Outline platelets.
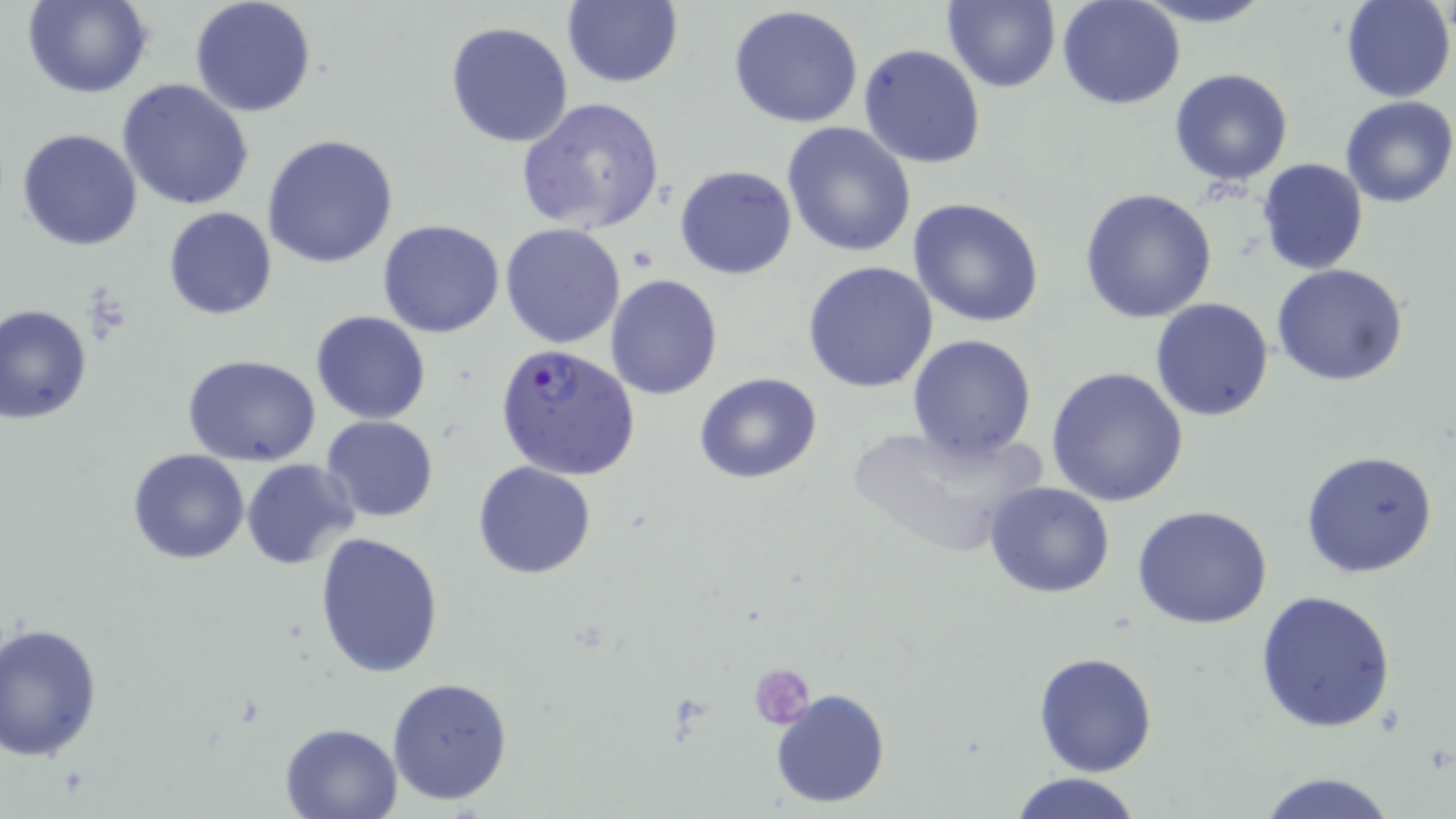
Approximate bounding boxes as (x1, y1, x2, y2) in pixels.
Platelets: (749, 662, 816, 729).

Plasmodium falciparum-infected red blood cell locations: (495, 343, 641, 479). Uninfected red blood cell locations: (24, 0, 152, 99), (188, 0, 317, 119), (561, 0, 683, 89), (940, 0, 1060, 92), (1056, 0, 1186, 111), (1128, 0, 1276, 28), (1340, 0, 1453, 103), (728, 6, 865, 128), (445, 21, 574, 149), (858, 43, 986, 168), (1169, 68, 1295, 186), (117, 79, 256, 212), (516, 96, 666, 235), (1339, 96, 1456, 207), (782, 122, 916, 257), (16, 127, 144, 250), (263, 133, 399, 268), (1258, 158, 1369, 275), (675, 165, 798, 280), (1080, 187, 1220, 324), (908, 197, 1045, 328), (163, 207, 276, 320), (378, 219, 505, 338), (500, 223, 627, 349), (803, 261, 939, 394), (1271, 263, 1409, 386), (605, 274, 723, 399), (1151, 299, 1275, 421), (0, 305, 93, 423), (310, 309, 432, 424), (907, 334, 1037, 461), (181, 354, 322, 467), (1045, 366, 1190, 506), (695, 373, 822, 484), (321, 415, 438, 523), (845, 418, 1050, 563), (128, 449, 249, 564), (1300, 450, 1439, 578), (241, 459, 360, 568), (474, 461, 596, 581), (984, 482, 1117, 600), (1133, 505, 1275, 629), (314, 532, 444, 677), (1255, 590, 1396, 733), (1, 622, 104, 764), (1033, 651, 1159, 776), (387, 677, 514, 806), (771, 688, 890, 809), (280, 721, 404, 818), (1010, 772, 1144, 819), (1254, 772, 1400, 819). Slide-level diagnosis: Plasmodium falciparum. Image is 1456×819 pixels. Single field of view. 1000x magnification. May-Grünwald-Giemsa-stained preparation. Optical microscopy. Thin blood film.